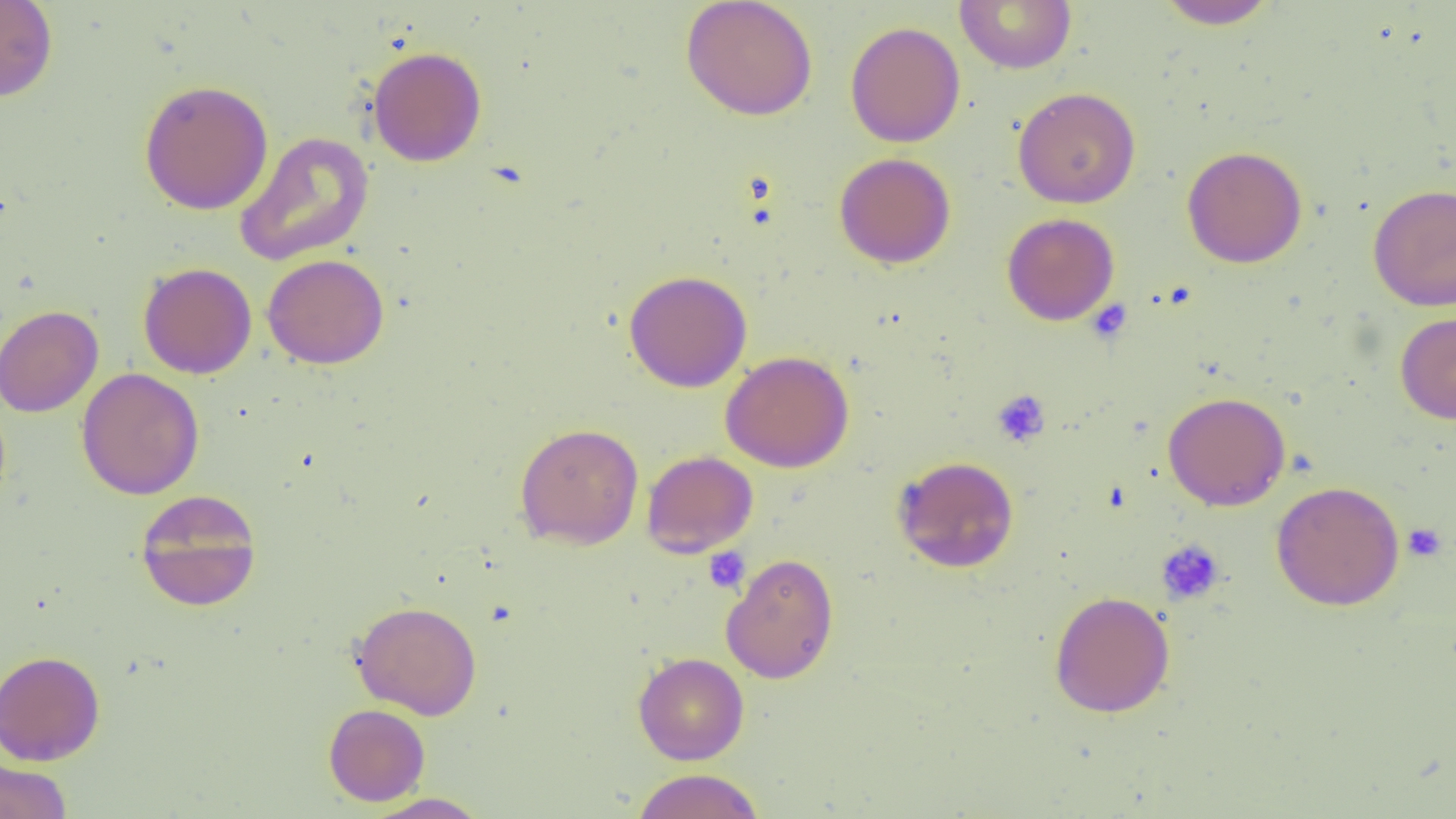

Approximate bounding boxes as (x1,y1)-(x2,y2) corner pairs in pixels. Platelet locations: (1087,299)-(1132,344), (992,390)-(1051,447), (1402,523)-(1447,562), (1156,539)-(1225,605), (703,547)-(751,594). Uninfected red blood cell locations: (0,0)-(58,102), (680,0)-(818,121), (955,0)-(1077,74), (1156,0)-(1279,30), (845,21)-(966,148), (367,45)-(487,167), (138,79)-(274,216), (1012,86)-(1141,209), (234,131)-(375,267), (1182,146)-(1308,268), (834,152)-(956,268), (1367,183)-(1456,311), (1001,213)-(1120,325), (262,253)-(389,369), (138,262)-(257,379), (623,270)-(752,392), (0,305)-(103,417), (1395,312)-(1456,424), (720,350)-(855,472), (76,368)-(205,500), (1162,391)-(1291,511), (514,422)-(644,549), (642,450)-(758,557), (892,455)-(1019,573), (1270,481)-(1405,610), (134,488)-(262,611), (721,552)-(839,684), (1049,590)-(1175,718), (351,600)-(482,720), (0,649)-(105,765), (632,652)-(749,765), (323,704)-(430,806), (0,758)-(72,819), (632,768)-(764,819), (361,792)-(492,818). Slide-level diagnosis: negative for blood parasites. Captured at 1000x magnification. Single field of view. Image is 1456×819 pixels. Thin blood smear. Light microscopy.